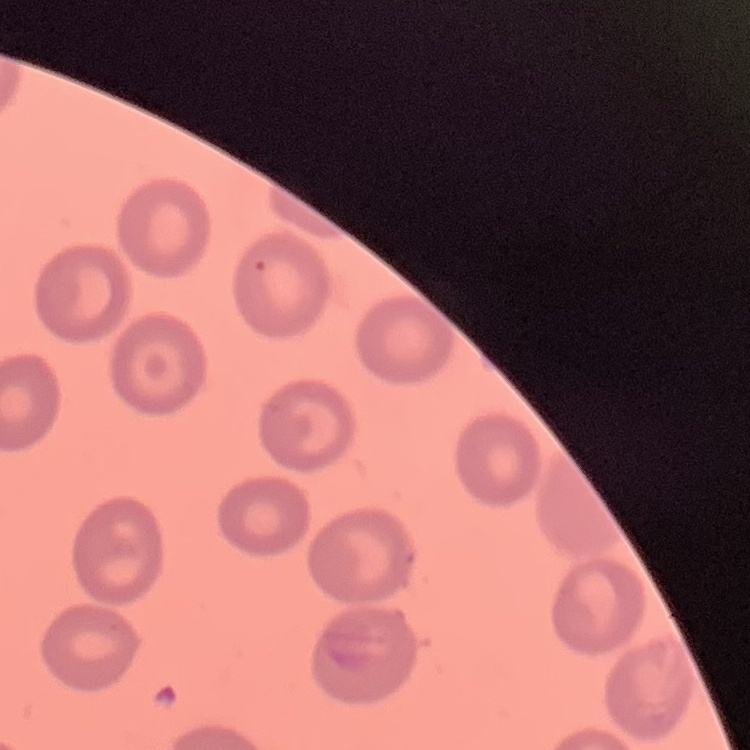 The red blood cells show no rouleaux formation. Thin blood smear. Stained with either Field's or Giemsa. One tile cut from a larger photomicrograph.